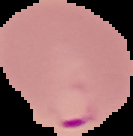
Summary:
  - Image type: segmented cell region with the area outside set to black
  - Image size: 133×136 pixels
  - Preparation: thin blood smear
  - Result: malaria parasites identified